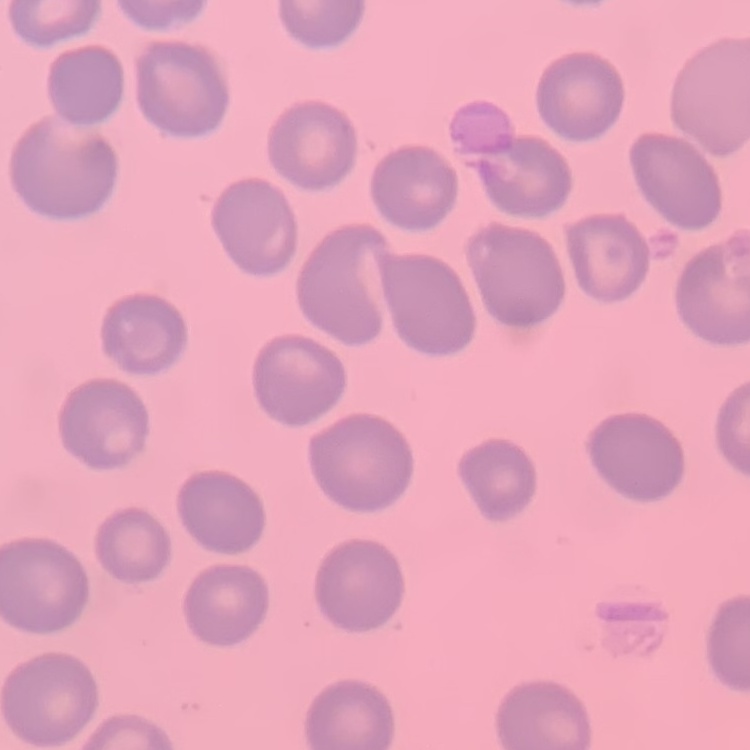

The red blood cells exhibit no rouleaux formation. One tile cut from a larger photomicrograph. Stained with either Field's or Giemsa. Thin blood smear.